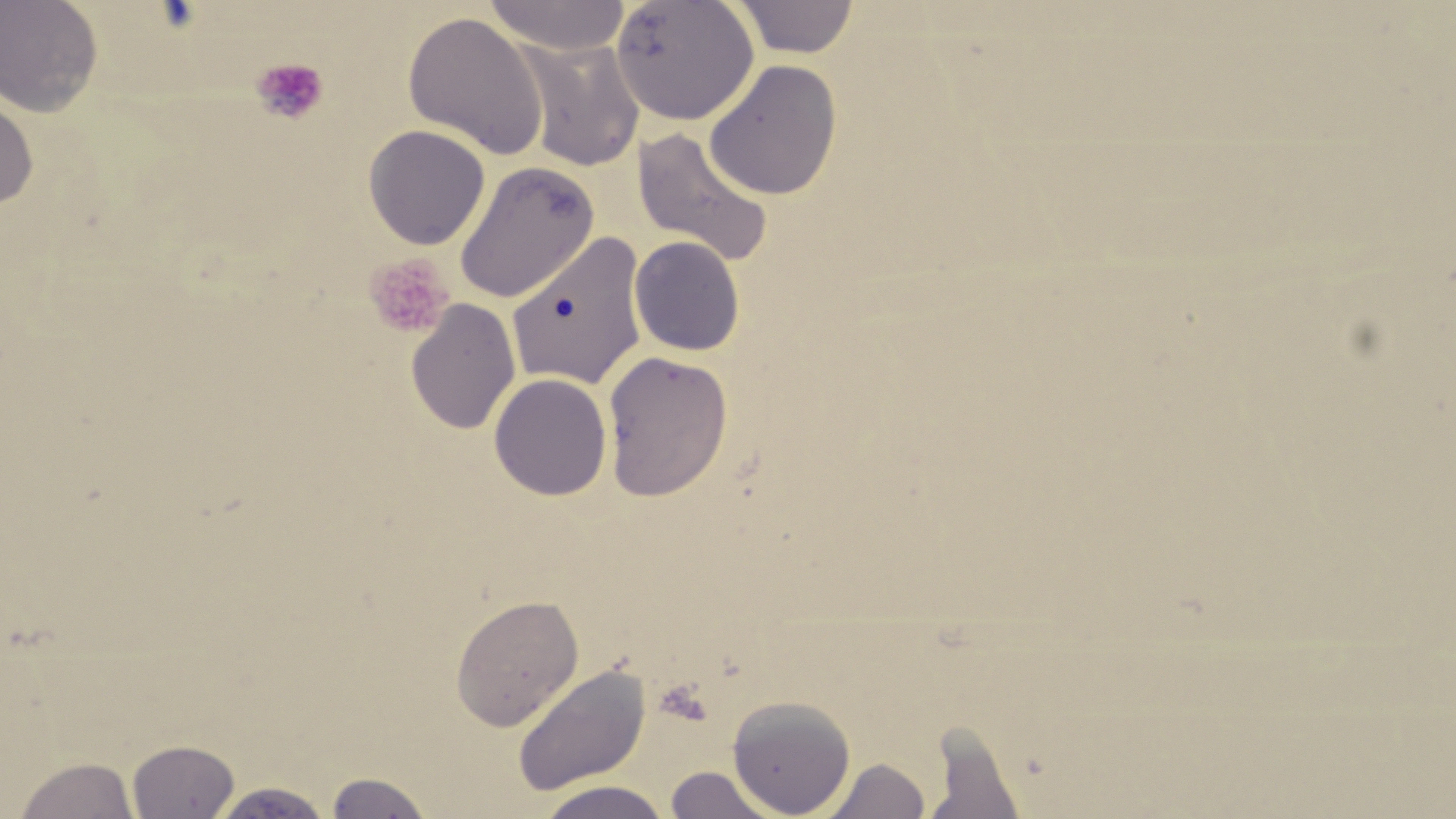

{
  "slide_level_diagnosis": "negative for blood parasites",
  "uninfected_red_blood_cell_locations": "approximate bounding boxes as named x1/y1/x2/y2 corners in pixels: (x1=0, y1=0, x2=104, y2=117), (x1=484, y1=0, x2=632, y2=55), (x1=611, y1=0, x2=760, y2=125), (x1=732, y1=0, x2=860, y2=59), (x1=401, y1=11, x2=549, y2=160), (x1=513, y1=35, x2=646, y2=172), (x1=704, y1=59, x2=842, y2=201), (x1=0, y1=91, x2=39, y2=210), (x1=363, y1=124, x2=490, y2=250), (x1=631, y1=127, x2=774, y2=268), (x1=454, y1=161, x2=599, y2=304), (x1=505, y1=231, x2=650, y2=391), (x1=629, y1=235, x2=746, y2=356), (x1=404, y1=298, x2=522, y2=436), (x1=601, y1=350, x2=734, y2=501), (x1=488, y1=373, x2=613, y2=501), (x1=449, y1=593, x2=584, y2=731), (x1=512, y1=662, x2=651, y2=797), (x1=726, y1=695, x2=856, y2=817), (x1=922, y1=724, x2=1028, y2=818), (x1=127, y1=739, x2=241, y2=818), (x1=14, y1=756, x2=139, y2=819), (x1=821, y1=757, x2=931, y2=818), (x1=664, y1=766, x2=781, y2=818), (x1=323, y1=771, x2=436, y2=818), (x1=534, y1=780, x2=674, y2=818), (x1=207, y1=781, x2=334, y2=818)",
  "image_size": "1456×819 pixels",
  "magnification": "1000x",
  "field_of_view": "single",
  "modality": "optical microscopy",
  "preparation": "thin blood film",
  "platelet_locations": "approximate bounding boxes as named x1/y1/x2/y2 corners in pixels: (x1=252, y1=56, x2=329, y2=126), (x1=363, y1=253, x2=453, y2=339)",
  "stain": "May-Grünwald-Giemsa"
}